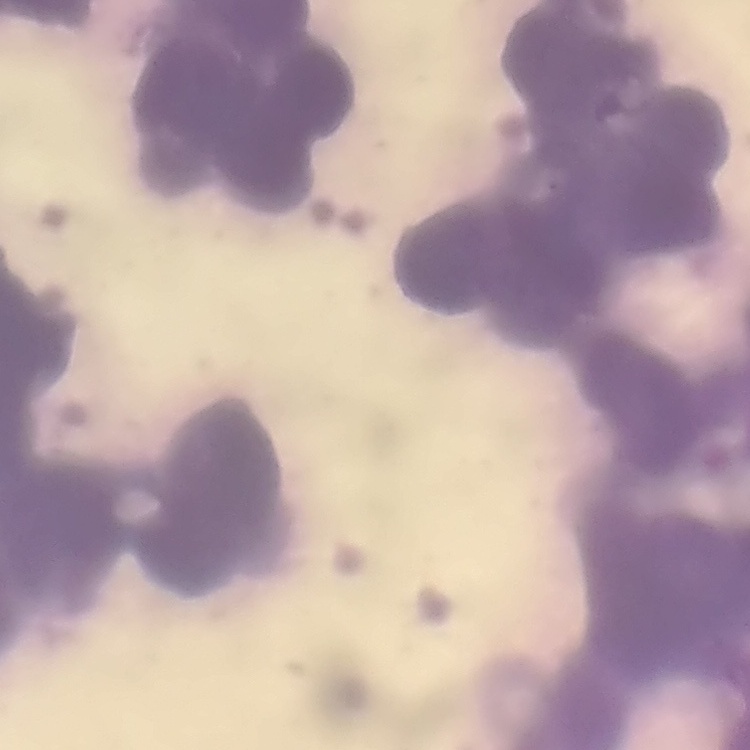
{
  "red_blood_cell_morphology": "rouleaux formation",
  "stain": "Field's or Giemsa",
  "preparation": "thin peripheral smear",
  "image_type": "square crop of a larger photomicrograph"
}